Give the position of every malaria parasite.
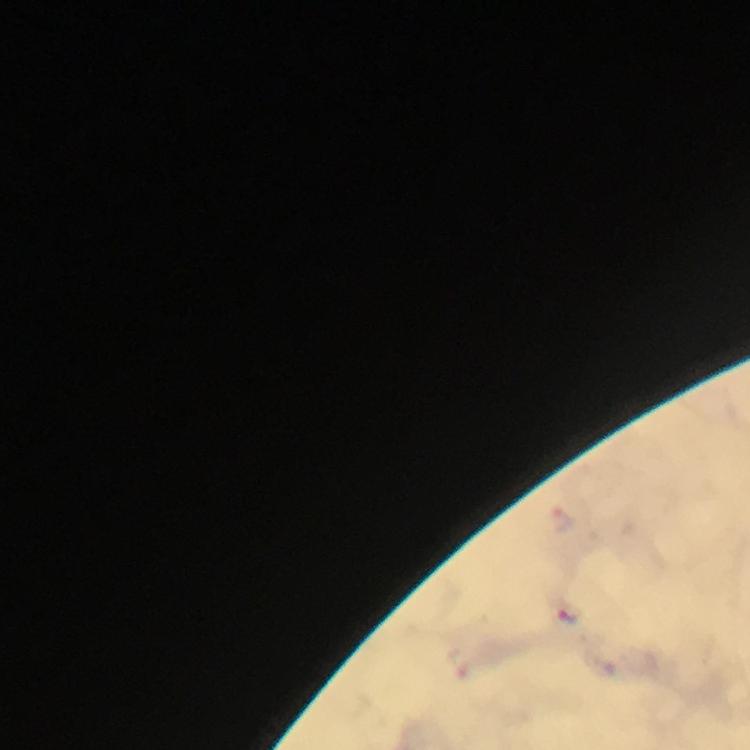
Approximate object centers, in pixels from the top-left corner.
Malaria parasites: (x=564, y=517).

Image is 750×750 pixels. From a diagnostic examination for malaria. Photographed with a smartphone mounted on the microscope. At 100x magnification. Thick blood smear. Cropped region of a single field of view. Immersion oil was used. Giemsa stain.